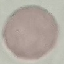
Malaria status: uninfected. Thin blood film. Photographed with a smartphone camera at the microscope eyepiece. Automatically extracted cell patch, resized to 64 × 64 pixels. Giemsa stain.